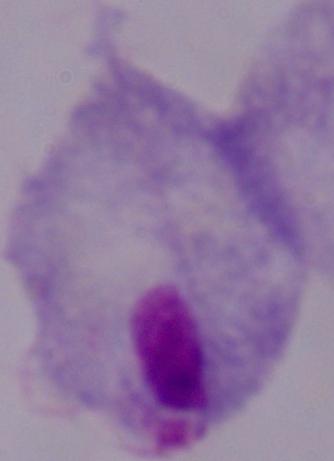

A trichomonad is seen. Micrograph. 1000x magnification.